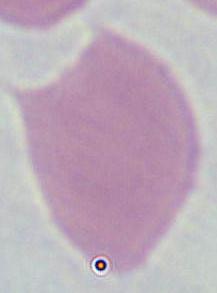 1000x magnification. Micrograph. An erythrocyte is seen.